Classify this cell by malaria status.
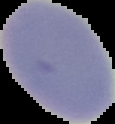

It is uninfected.

The area outside the segmented cell region is set to black. Image is 115×124 pixels. From a thin blood film.